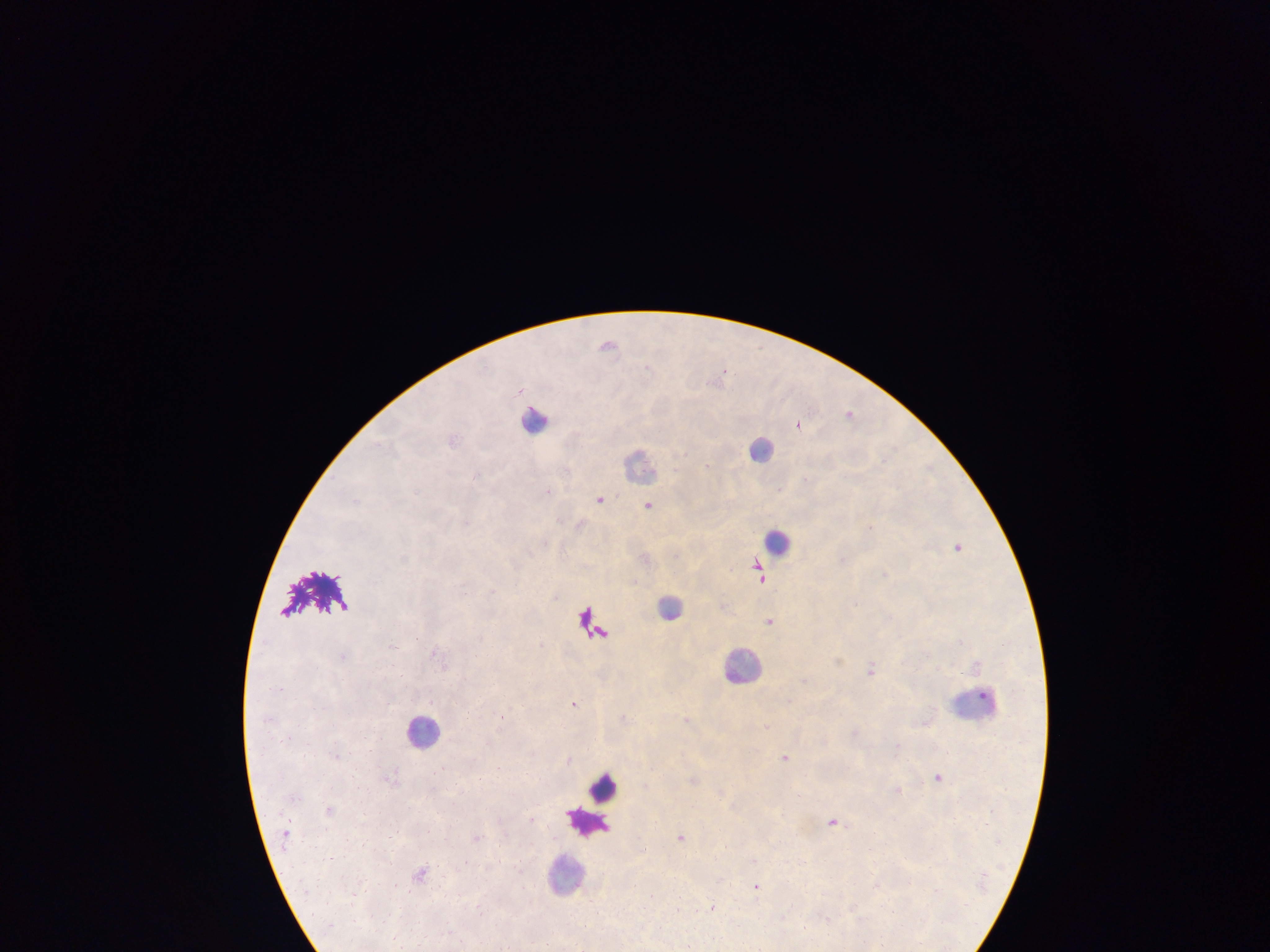

capture = mobile-phone photograph through a microscope
malaria parasite locations = approximate centers as x y in pixels: 608 343; 724 367; 647 369; 849 415; 798 423; 709 464; 478 474; 416 490; 548 491; 599 500; 647 504; 957 547; 404 558; 757 565; 885 576; 762 580; 464 592; 494 592; 770 622; 961 641; 393 647; 436 652; 342 656; 839 661; 871 671; 983 697; 575 704; 532 752; 336 756; 786 757; 569 760; 497 767; 937 777; 900 789; 835 823; 682 836; 421 871; 396 884; 757 886
field of view = single
image size = 1270×952 pixels
preparation = thick blood film
leukocyte locations = approximate centers as x y in pixels: 534 418; 763 451; 641 467; 775 541; 671 608; 740 664; 423 731; 601 785; 583 819; 566 873
country = Ghana